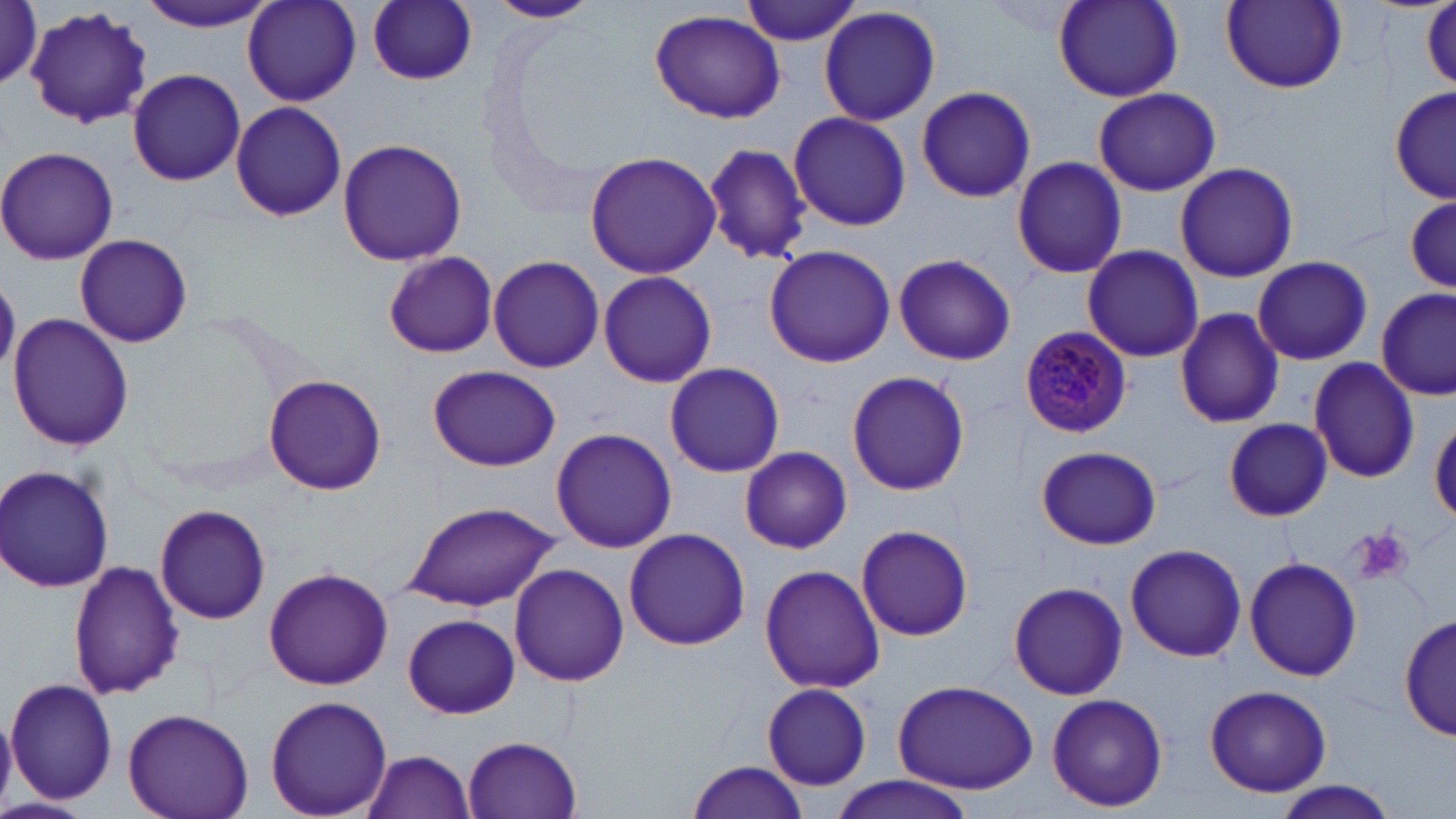
Summary:
  - Coordinate format: approximate bounding boxes as named x1/y1/x2/y2 corners in pixels
  - Plasmodium malariae-infected red blood cell locations: (x1=1018, y1=326, x2=1133, y2=437)
  - Platelet locations: (x1=1352, y1=527, x2=1414, y2=587)
  - Uninfected red blood cell locations: (x1=136, y1=0, x2=276, y2=32), (x1=242, y1=0, x2=361, y2=105), (x1=488, y1=0, x2=601, y2=23), (x1=740, y1=0, x2=865, y2=46), (x1=1053, y1=0, x2=1184, y2=101), (x1=367, y1=1, x2=478, y2=86), (x1=1220, y1=1, x2=1347, y2=93), (x1=3, y1=2, x2=44, y2=90), (x1=1420, y1=3, x2=1455, y2=94), (x1=818, y1=6, x2=942, y2=126), (x1=25, y1=7, x2=154, y2=132), (x1=650, y1=9, x2=787, y2=124), (x1=127, y1=68, x2=246, y2=187), (x1=1393, y1=85, x2=1456, y2=202), (x1=1093, y1=86, x2=1221, y2=196), (x1=916, y1=87, x2=1038, y2=204), (x1=230, y1=101, x2=346, y2=223), (x1=788, y1=112, x2=912, y2=231), (x1=336, y1=136, x2=468, y2=266), (x1=704, y1=143, x2=812, y2=264), (x1=0, y1=146, x2=119, y2=265), (x1=584, y1=150, x2=722, y2=280), (x1=1011, y1=156, x2=1129, y2=280), (x1=1173, y1=161, x2=1301, y2=283), (x1=1404, y1=192, x2=1453, y2=297), (x1=75, y1=233, x2=193, y2=348), (x1=763, y1=244, x2=896, y2=369), (x1=1081, y1=244, x2=1204, y2=362), (x1=382, y1=250, x2=499, y2=359), (x1=892, y1=252, x2=1018, y2=367), (x1=488, y1=254, x2=605, y2=374), (x1=1253, y1=255, x2=1374, y2=366), (x1=597, y1=271, x2=718, y2=388), (x1=1377, y1=289, x2=1453, y2=400), (x1=1173, y1=306, x2=1284, y2=429), (x1=7, y1=314, x2=132, y2=449), (x1=1308, y1=356, x2=1420, y2=482), (x1=665, y1=361, x2=785, y2=478), (x1=428, y1=364, x2=560, y2=472), (x1=847, y1=369, x2=971, y2=497), (x1=263, y1=374, x2=387, y2=496), (x1=1224, y1=418, x2=1332, y2=520), (x1=1431, y1=418, x2=1456, y2=524), (x1=551, y1=426, x2=677, y2=553), (x1=1035, y1=445, x2=1162, y2=550), (x1=741, y1=446, x2=852, y2=554), (x1=0, y1=463, x2=116, y2=595), (x1=401, y1=501, x2=562, y2=612), (x1=154, y1=502, x2=272, y2=625), (x1=855, y1=524, x2=974, y2=641), (x1=623, y1=528, x2=750, y2=650), (x1=1126, y1=542, x2=1247, y2=663), (x1=1244, y1=556, x2=1362, y2=682), (x1=68, y1=561, x2=184, y2=700), (x1=508, y1=563, x2=629, y2=686), (x1=760, y1=564, x2=884, y2=693), (x1=264, y1=567, x2=393, y2=691), (x1=1007, y1=580, x2=1128, y2=700), (x1=1400, y1=612, x2=1454, y2=742), (x1=403, y1=614, x2=519, y2=718), (x1=6, y1=678, x2=117, y2=806), (x1=893, y1=680, x2=1039, y2=793), (x1=762, y1=684, x2=872, y2=789), (x1=1205, y1=684, x2=1332, y2=798), (x1=1046, y1=692, x2=1169, y2=812), (x1=265, y1=695, x2=392, y2=818), (x1=123, y1=708, x2=253, y2=819), (x1=462, y1=735, x2=582, y2=818), (x1=362, y1=751, x2=477, y2=819), (x1=685, y1=760, x2=809, y2=819), (x1=826, y1=775, x2=975, y2=818), (x1=1270, y1=782, x2=1399, y2=817), (x1=0, y1=796, x2=89, y2=819)
  - Slide-level diagnosis: Plasmodium malariae
  - Magnification: 1000x
  - Preparation: thin blood smear
  - Image size: 1456×819 pixels
  - Modality: optical microscopy
  - Stain: May-Grünwald-Giemsa
  - Field of view: single